Name the parasite shown.
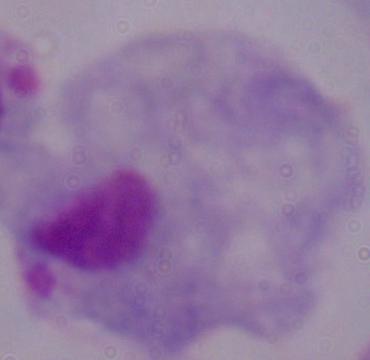

A trichomonad.

Summary:
  - Modality: micrograph
  - Magnification: 1000x